Point out each Plasmodium parasite.
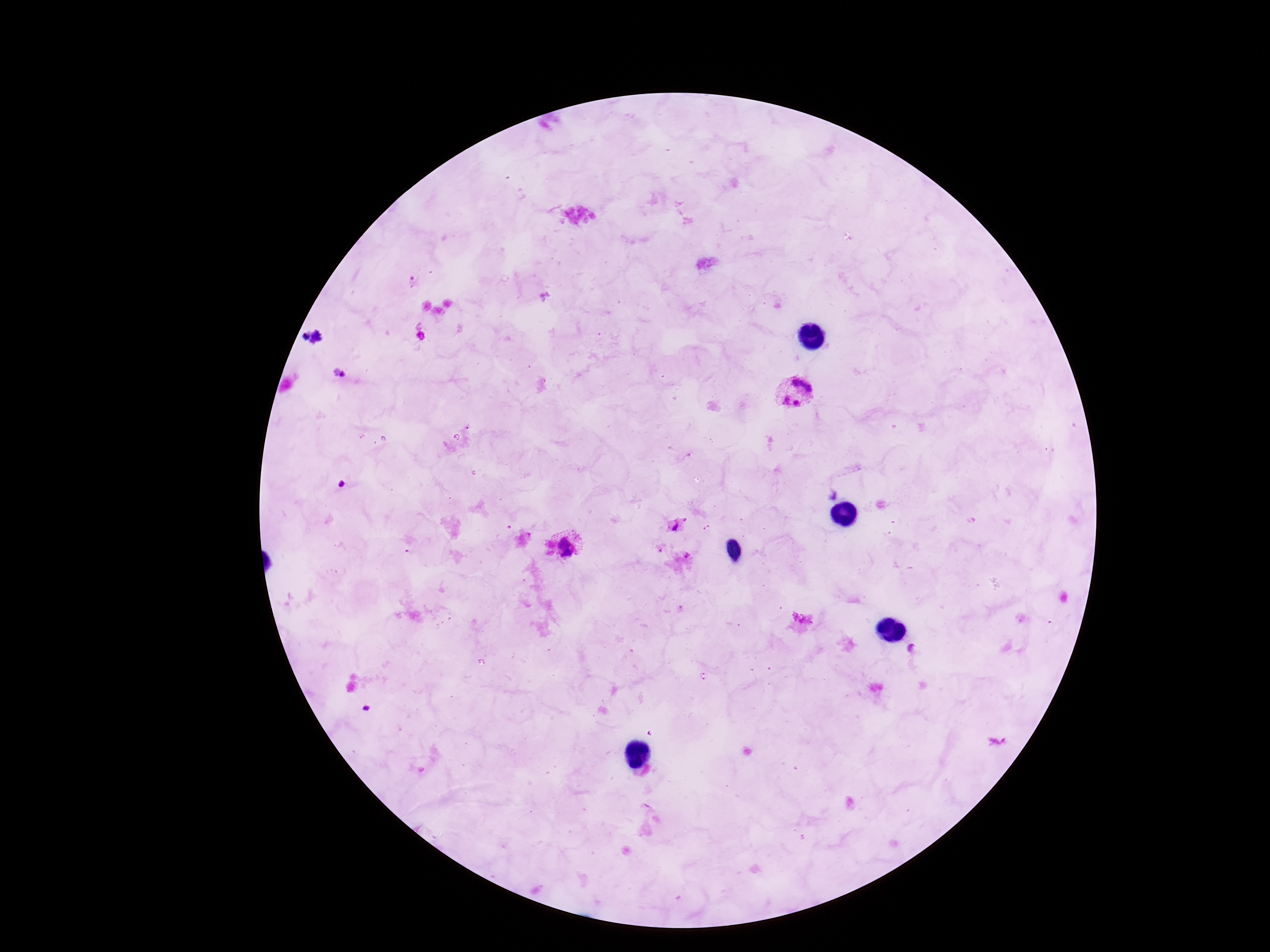
Approximate centers as (x, y) in pixels.
Plasmodium parasites: (340, 375), (796, 391), (675, 527), (565, 547).

capture: smartphone camera through the microscope eyepiece
image_size: 1270×952 pixels
stain: Giemsa
magnification: 100x
patient_malaria_status: positive
preparation: thick blood film
field_of_view: one from this slide